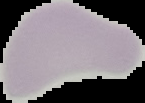 Image is 145×103 pixels. From a thin blood film. Segmented cell region on a black background. Result: negative for malaria parasites.